Give the preparation type.
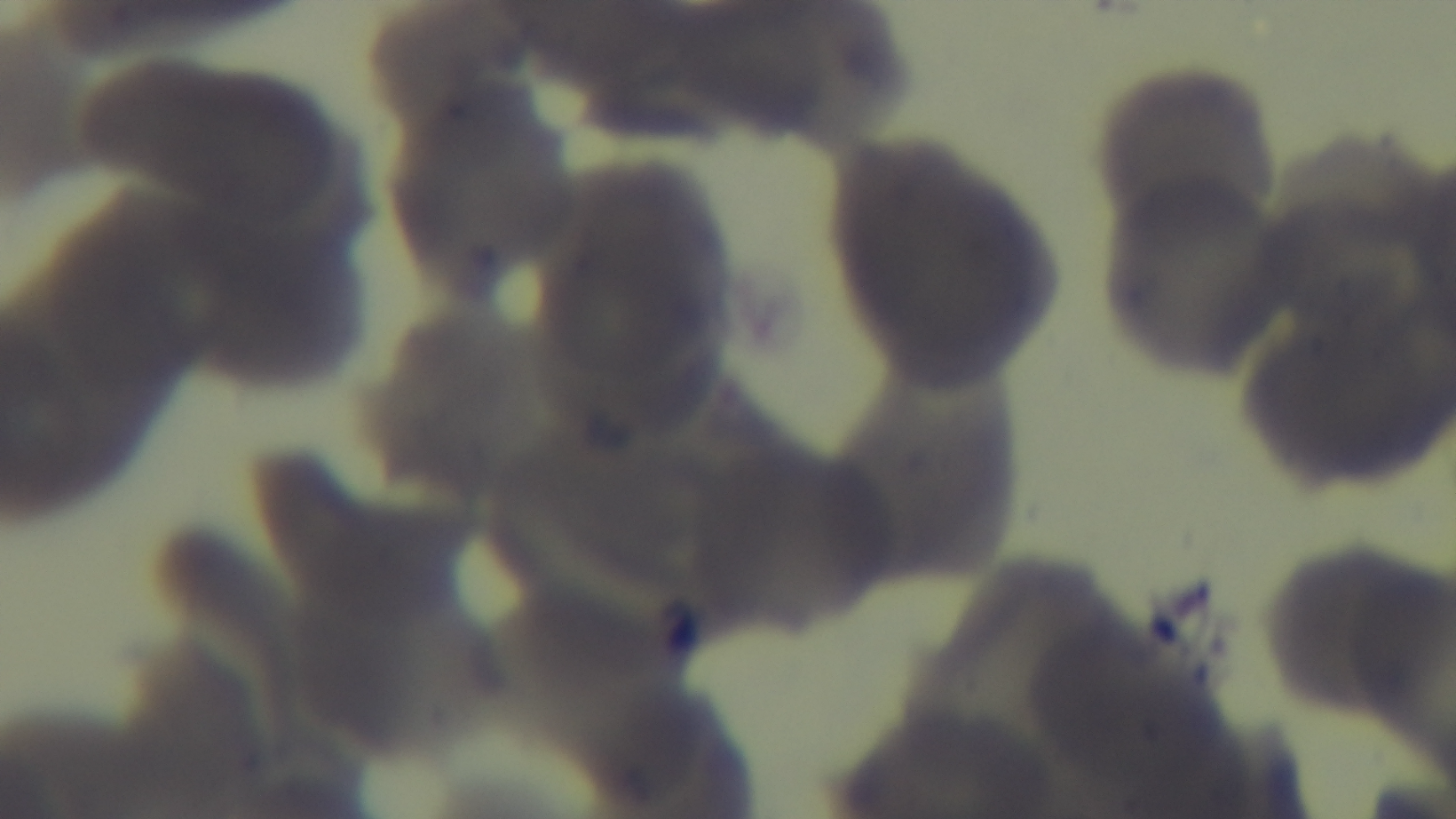

It is a thin blood film.

objective = 100x oil immersion
malaria status = uninfected
field of view = one from the slide
stain = Giemsa
capture = mounted 4K digital camera
modality = light microscopy